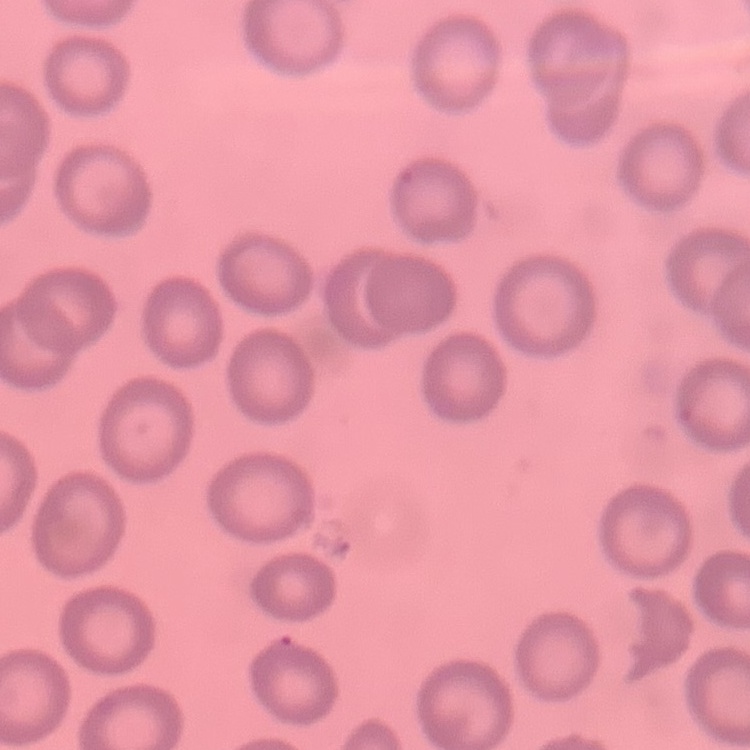
Summary:
  - Erythrocyte morphology: no rouleaux formation
  - Image type: square crop of a larger photomicrograph
  - Preparation: thin blood film
  - Stain: Field's or Giemsa